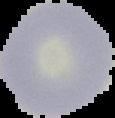
From a thin blood film. Segmented cell region on a black background. Image is 115×118 pixels. Malaria status: uninfected.